Give the position of every Plasmodium parasite visible.
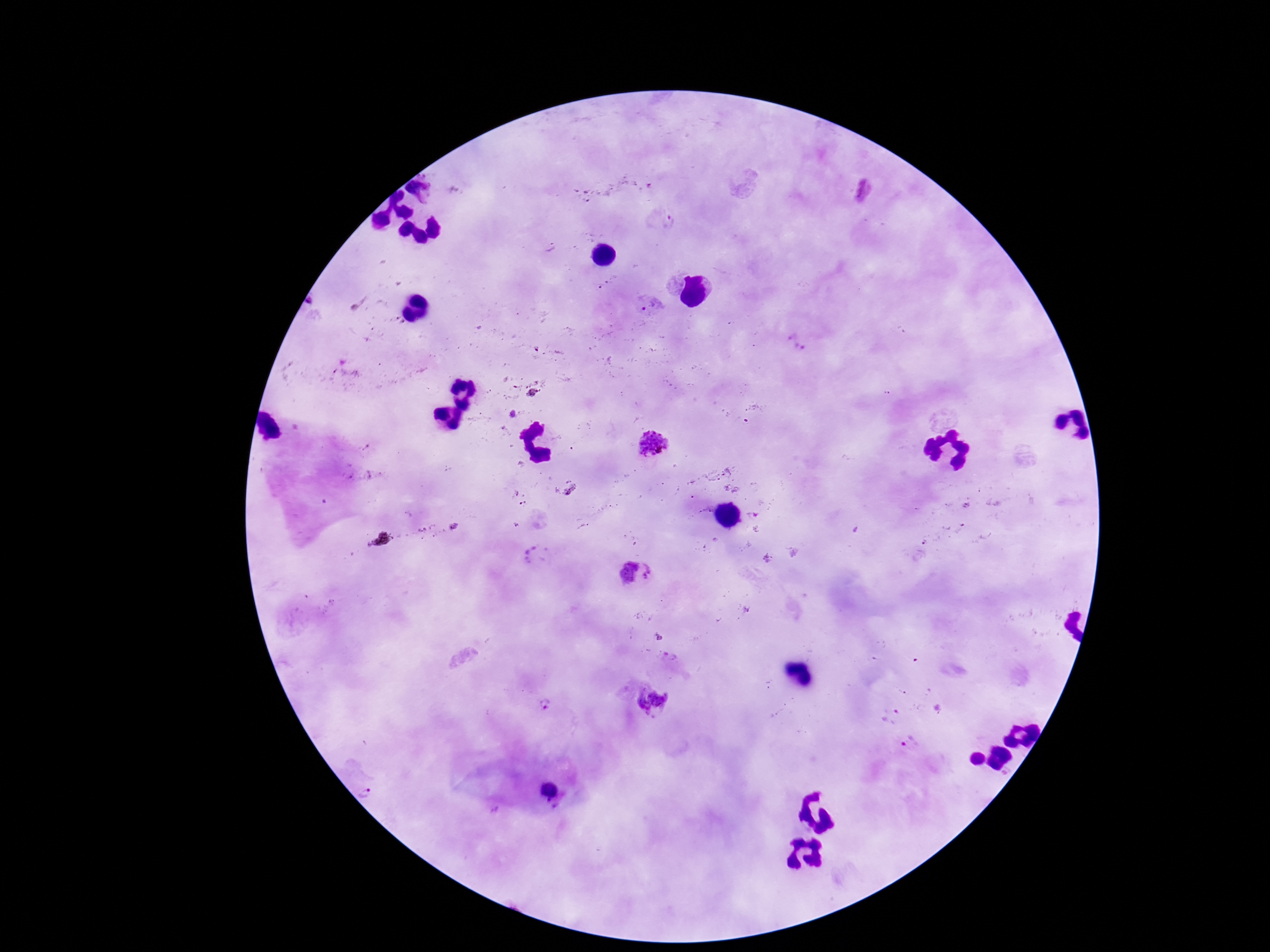

Approximate centers as [x, y] in pixels.
Plasmodium parasites: [652, 187], [863, 190], [662, 218], [550, 247], [647, 302], [795, 343], [533, 394], [513, 414], [652, 445], [752, 515], [531, 554], [768, 559], [635, 574], [671, 656], [653, 701], [545, 706], [910, 742], [974, 759], [548, 790], [367, 794], [495, 810].

{
  "image_size": "1270×952 pixels",
  "field_of_view": "single",
  "patient_malaria_status": "positive",
  "preparation": "thick blood smear",
  "capture": "smartphone camera through the microscope eyepiece",
  "magnification": "100x",
  "stain": "Giemsa"
}